Classify this cell by malaria status.
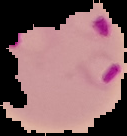

It is parasitized.

{
  "image_type": "segmented cell region on a black background",
  "image_size": "127×136 pixels",
  "preparation": "thin blood film"
}